Outline every parasitised red blood cell.
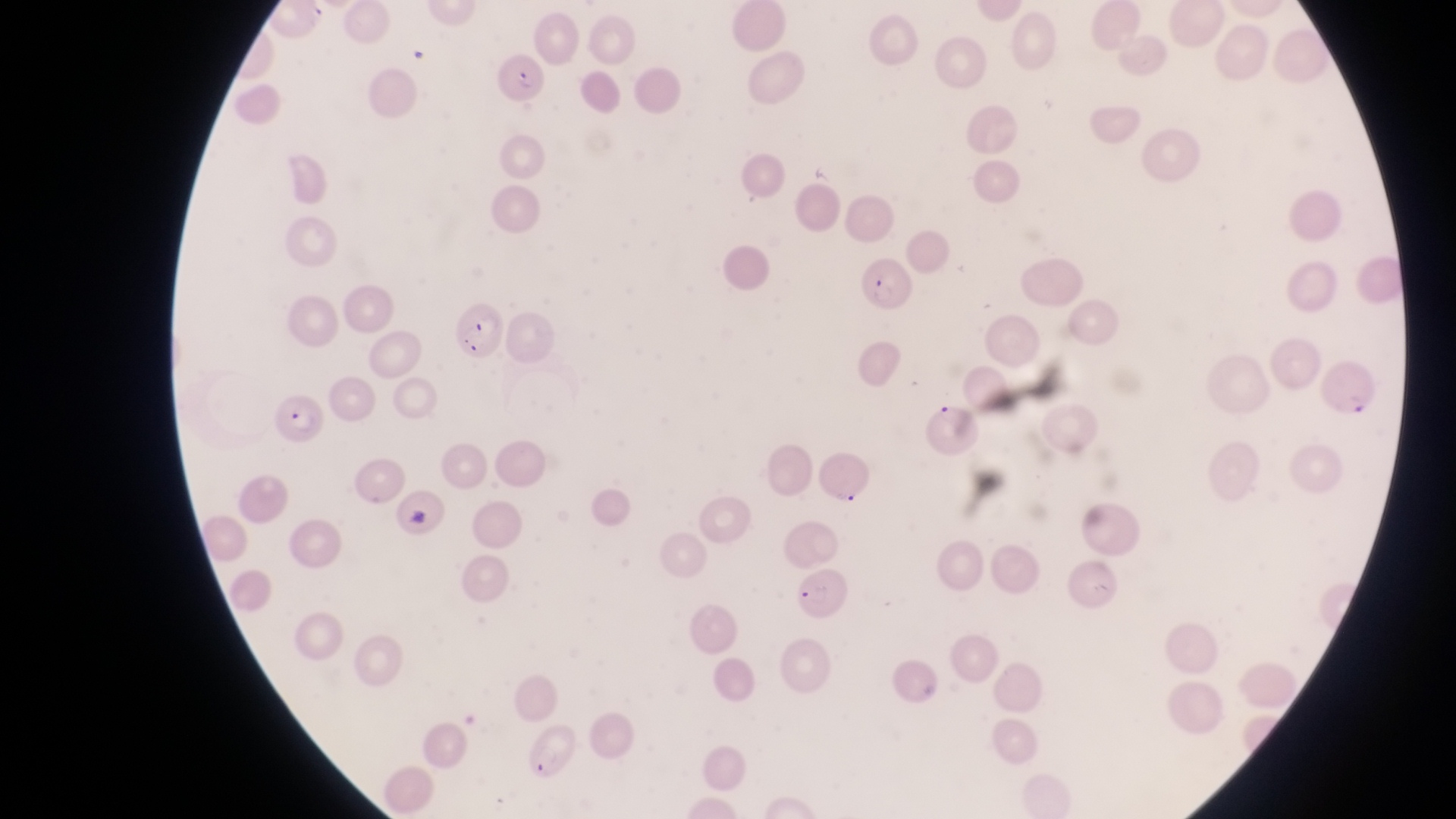

Approximate bounding boxes as left top right bottom in pixels.
Parasitised red blood cells: 495 46 555 107; 858 253 914 312; 446 297 506 360; 1323 359 1378 419; 274 394 329 444; 788 566 859 622; 519 727 583 786.

Summary:
  - Artifact (platelet-like body, stain precipitate, or debris) locations: 406 34 435 70; 402 499 434 533
  - Magnification: 1000x
  - Capture: smartphone photograph through the eyepiece of an Olympus CX-23 microscope
  - Image size: 1456×819 pixels
  - Field of view: single
  - Preparation: thin blood smear
  - Country: Uganda